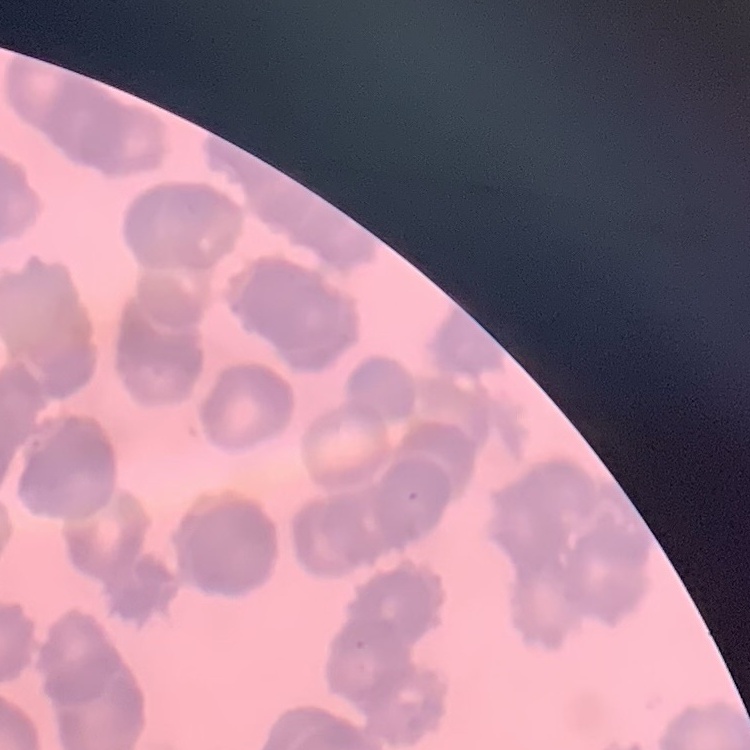
red blood cell morphology = rouleaux formation
preparation = thin blood smear
stain = Field's or Giemsa
image type = square crop of a larger photomicrograph